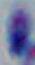 Captured at 1000x magnification. Toxoplasma gondii is shown. Photomicrograph.